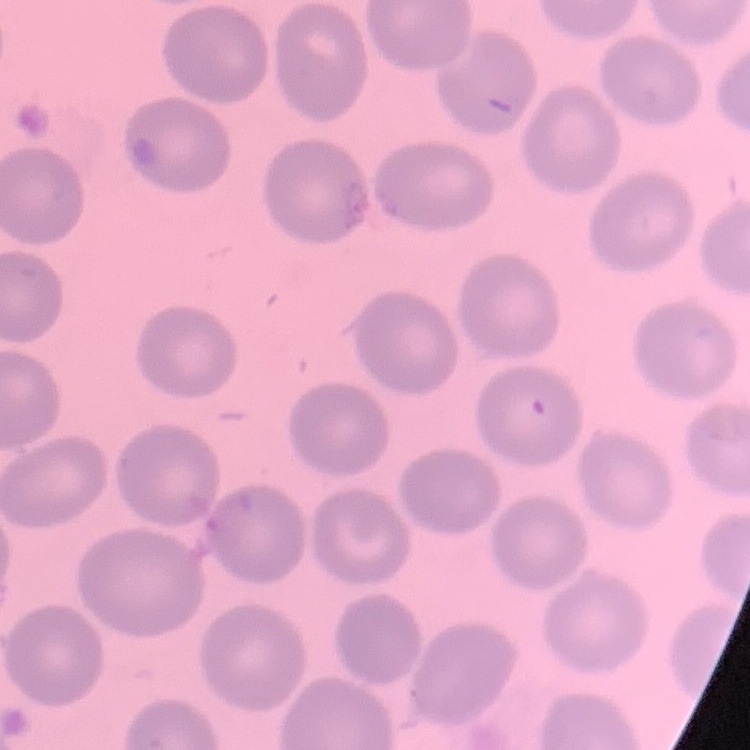

Summary:
  - Erythrocyte morphology: no rouleaux formation
  - Preparation: thin blood smear
  - Image type: square crop of a larger photomicrograph
  - Stain: Field's or Giemsa